Locate every blood parasite and identify its species.
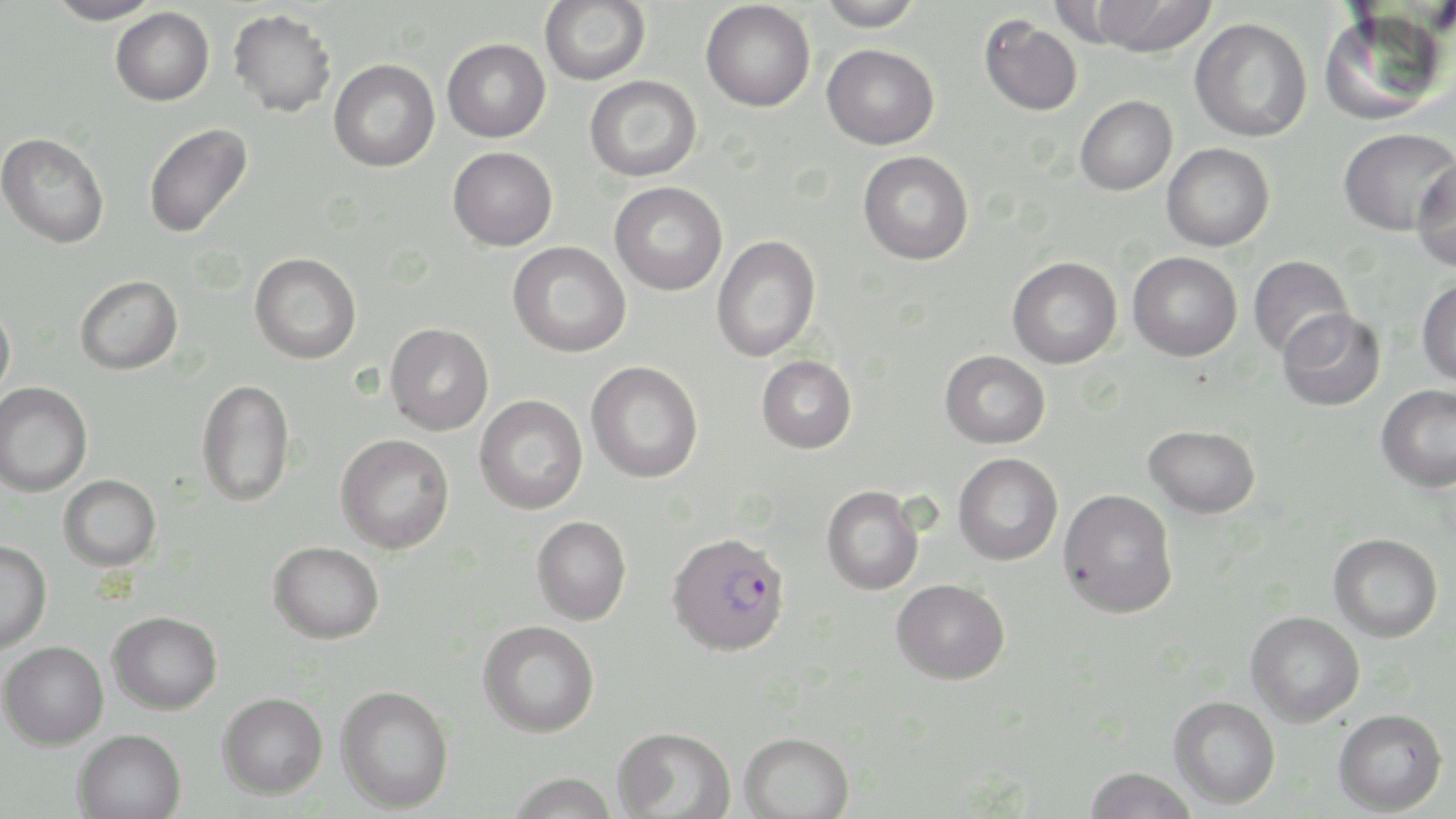

Approximate bounding boxes as (x1,y1)-(x2,y2) corner pairs in pixels.
Plasmodium falciparum-infected red blood cells: (666,531)-(791,656).
No Plasmodium ovale, Plasmodium malariae, Plasmodium vivax, Babesia divergens, or Trypanosoma brucei observed.

Summary:
  - Uninfected red blood cell locations: (46,0)-(162,26), (540,0)-(650,85), (818,0)-(924,31), (1090,0)-(1219,58), (701,1)-(815,112), (110,7)-(215,106), (1319,7)-(1449,127), (227,9)-(336,118), (979,16)-(1083,116), (1189,17)-(1312,142), (442,38)-(551,142), (822,44)-(939,149), (329,58)-(440,172), (585,75)-(702,182), (1075,95)-(1177,195), (143,123)-(253,239), (1339,127)-(1456,235), (0,132)-(109,248), (1162,143)-(1274,251), (448,146)-(558,250), (858,150)-(974,265), (1412,156)-(1456,273), (609,181)-(727,295), (711,235)-(821,362), (508,241)-(631,357), (1127,251)-(1242,361), (249,252)-(361,364), (1248,255)-(1353,359), (1007,256)-(1122,369), (75,275)-(183,375), (1417,278)-(1456,386), (0,300)-(16,404), (1278,309)-(1385,411), (385,323)-(494,436), (940,350)-(1050,448), (757,355)-(857,453), (586,361)-(703,483), (196,379)-(295,507), (0,382)-(92,498), (1376,384)-(1456,492), (474,394)-(588,515), (1144,424)-(1260,518), (335,434)-(454,554), (953,452)-(1063,565), (58,474)-(162,572), (821,485)-(925,595), (1058,489)-(1178,618), (532,515)-(631,625), (1328,533)-(1443,642), (0,540)-(51,654), (269,540)-(384,643), (892,578)-(1010,684), (108,610)-(223,714), (1245,611)-(1365,727), (478,620)-(600,737), (0,640)-(109,750), (335,685)-(454,813), (218,691)-(328,799), (1169,695)-(1281,809), (1333,708)-(1447,815), (612,726)-(736,819), (74,728)-(187,819), (738,731)-(854,819), (1083,766)-(1198,819), (508,772)-(619,818)
  - Slide-level diagnosis: Plasmodium falciparum
  - Modality: optical microscopy
  - Stain: May-Grünwald-Giemsa
  - Magnification: 1000x
  - Preparation: thin blood film
  - Field of view: single
  - Image size: 1456×819 pixels